State which cell type is depicted.
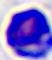

This is a leukocyte.

400x magnification. Micrograph.